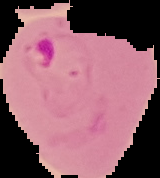
Summary:
  - Image size: 160×178 pixels
  - Preparation: thin blood film
  - Malaria status: parasitized
  - Image type: segmented cell region on a black background